Identify the parasite.
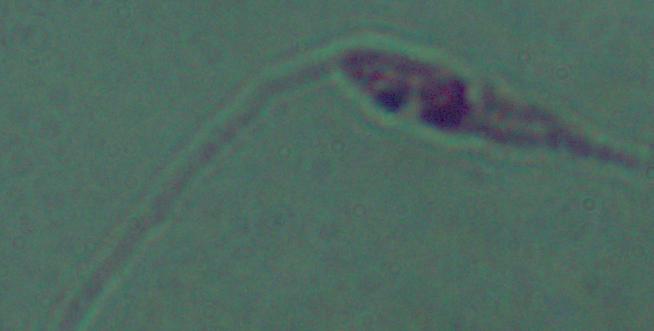

This is Leishmania.

Summary:
  - Modality: photomicrograph
  - Magnification: 1000x